Assess the morphology of the erythrocytes.
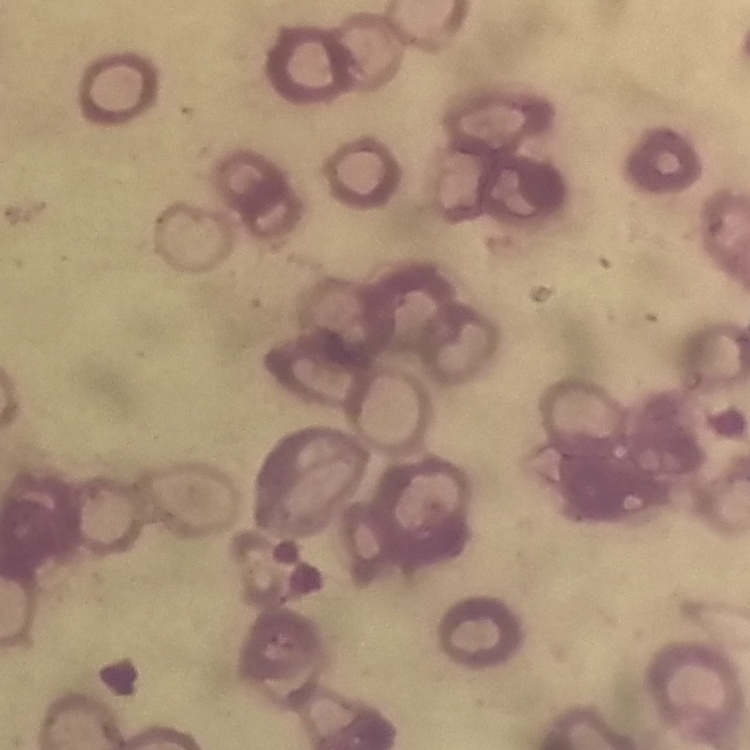

Rouleaux formation.

Thin peripheral smear. Field's or Giemsa stain. One tile cut from a larger photomicrograph.